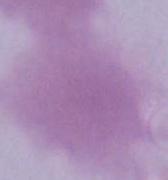

modality = micrograph
magnification = 1000x
identification = red blood cell